Name the blood parasite species.
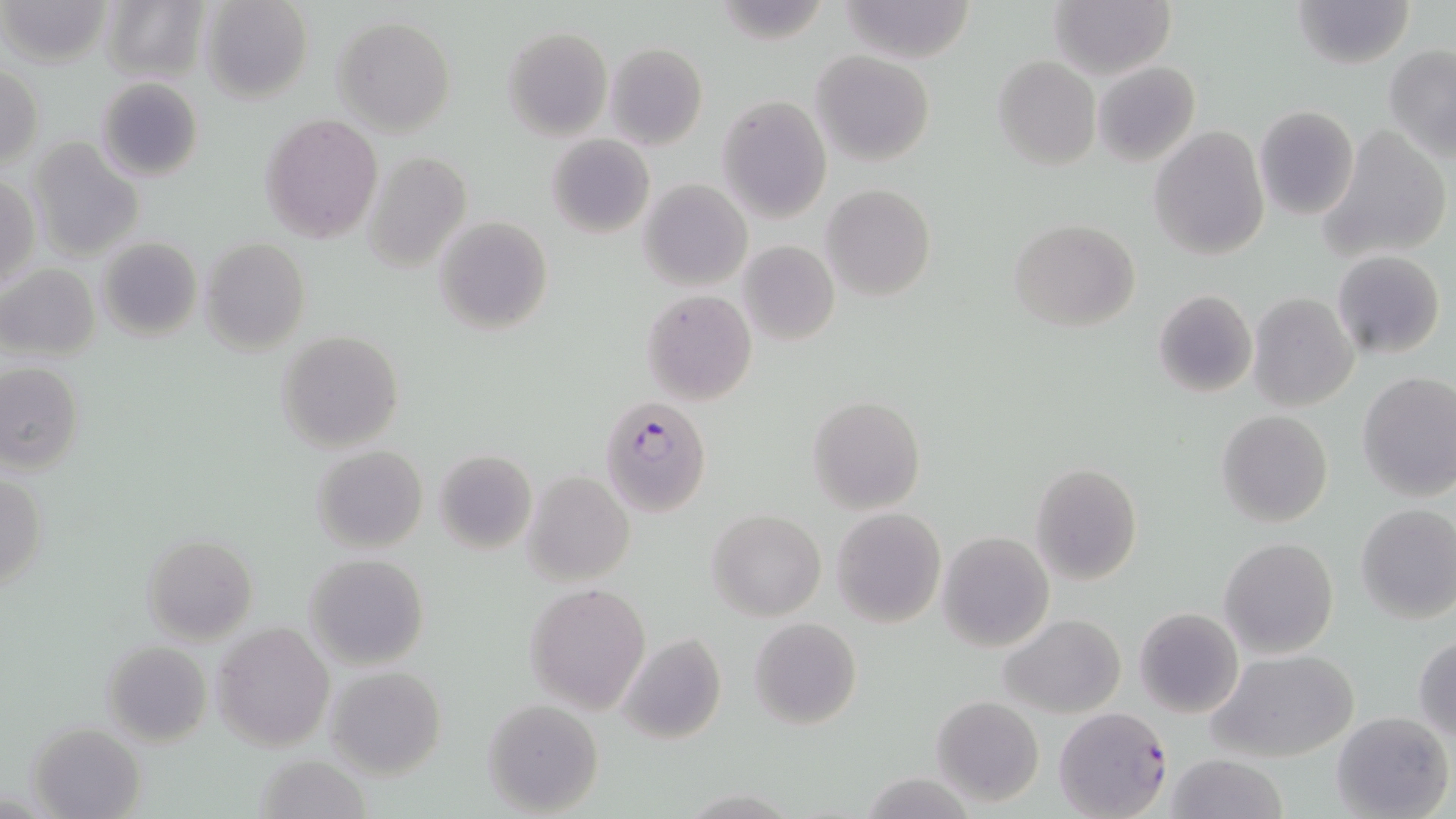
Plasmodium falciparum.

Approximate bounding boxes as (x1,y1)-(x2,y2) corner pairs in pixels. Uninfected red blood cell locations: (3,0)-(113,69), (200,0)-(313,104), (837,0)-(979,63), (1051,0)-(1176,79), (1291,0)-(1414,71), (101,1)-(208,84), (333,15)-(456,135), (502,26)-(612,138), (604,43)-(708,149), (1384,43)-(1456,161), (812,50)-(934,167), (992,56)-(1101,170), (1094,61)-(1200,168), (1,64)-(44,169), (95,77)-(206,182), (718,95)-(831,222), (1253,105)-(1360,221), (259,113)-(383,244), (1149,125)-(1269,260), (1319,126)-(1451,263), (546,133)-(655,238), (27,140)-(144,263), (361,148)-(472,271), (0,177)-(39,291), (638,178)-(753,291), (822,184)-(935,301), (433,217)-(553,336), (1009,218)-(1139,333), (96,236)-(202,342), (199,237)-(313,356), (738,240)-(840,346), (1331,250)-(1446,359), (1,263)-(101,362), (641,289)-(757,404), (1152,289)-(1258,399), (1247,292)-(1358,412), (276,330)-(404,454), (0,361)-(85,474), (1357,370)-(1456,500), (807,395)-(925,514), (1216,409)-(1334,528), (313,446)-(427,553), (435,449)-(536,553), (1031,463)-(1142,585), (1,469)-(47,594), (522,471)-(634,585), (1355,504)-(1456,623), (831,507)-(946,628), (707,509)-(825,622), (938,531)-(1053,651), (142,534)-(259,644), (1219,536)-(1340,659), (303,553)-(431,671), (525,582)-(651,714), (1134,607)-(1243,719), (1000,613)-(1125,718), (749,617)-(862,731), (213,621)-(335,753), (615,632)-(726,746), (1413,633)-(1456,742), (101,640)-(212,747), (1211,648)-(1359,763), (326,666)-(446,781), (931,695)-(1044,808), (482,699)-(605,817), (1331,710)-(1452,819), (27,722)-(146,819), (254,752)-(371,819), (1165,754)-(1290,819), (862,774)-(975,817). Plasmodium falciparum-infected red blood cell locations: (599,397)-(712,517), (1053,703)-(1173,819). May-Grünwald-Giemsa-stained preparation. Thin blood smear. Optical microscopy. Image is 1456×819 pixels. Captured at 1000x magnification. One field of a larger specimen.